Identify the preparation type.
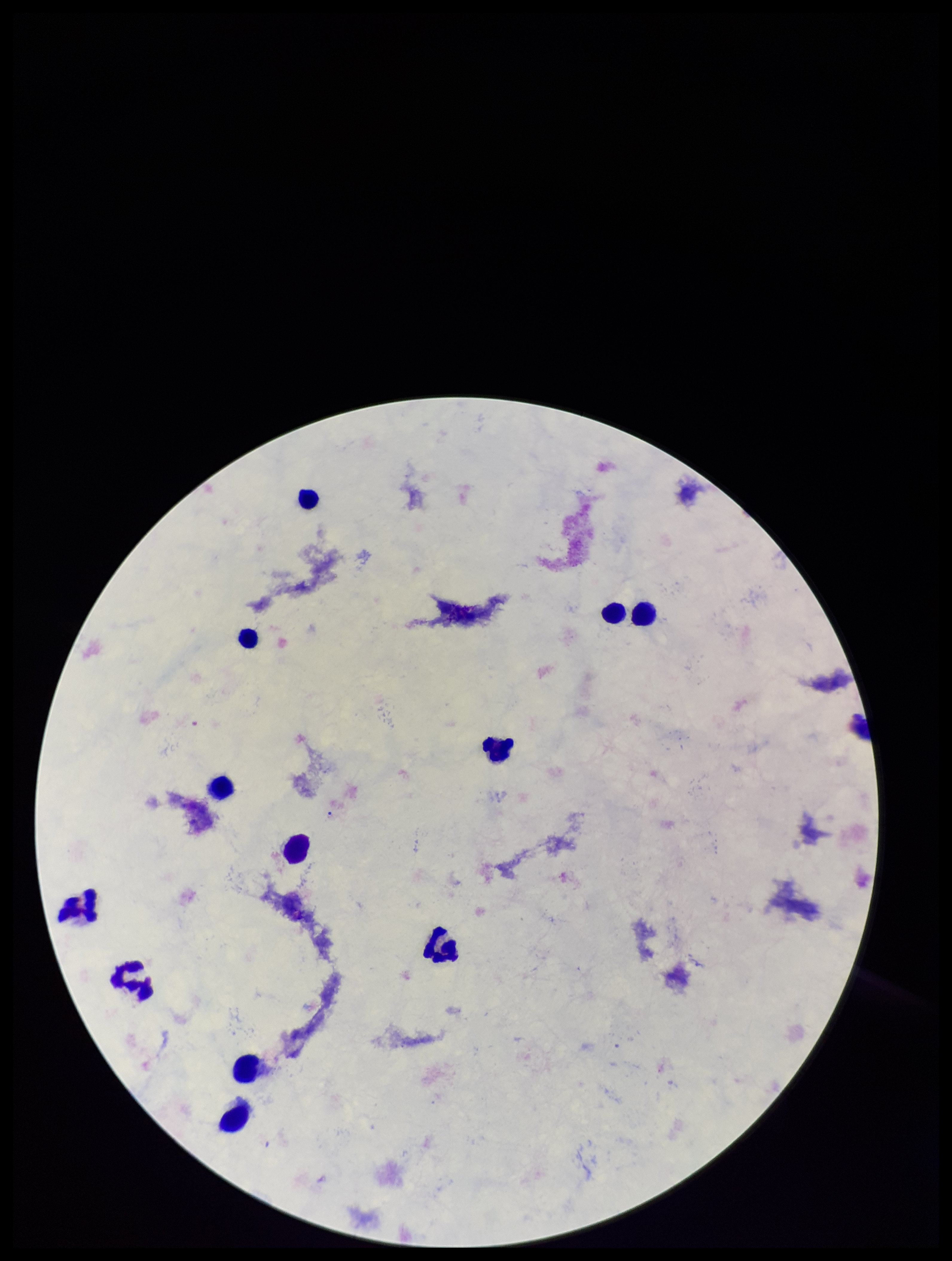
Thick.

Leukocyte count: 12. Patient malaria status: negative. Image is 952×1261 pixels. Plasmodium parasites: none detected. Stained with Giemsa. Single field of view. Parasite count: 0. Photographed through the microscope eyepiece with a smartphone camera.